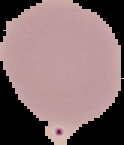

Summary:
  - Image type: segmented cell region with the area outside set to black
  - Preparation: thin blood film
  - Malaria status: uninfected
  - Image size: 124×145 pixels